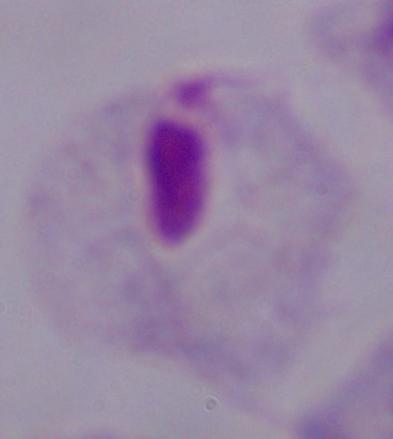

magnification = 1000x
identification = trichomonad
modality = micrograph